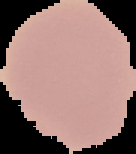

image size = 136×154 pixels
malaria status = uninfected
preparation = thin blood film
image type = cell region segmented out of the field of view; surrounding area masked to black